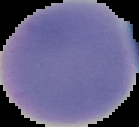
preparation = thin blood smear
image type = segmented cell region with the area outside set to black
image size = 139×127 pixels
result = negative for malaria parasites